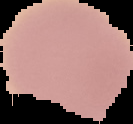
preparation = thin blood smear
image type = segmented cell region with the area outside set to black
malaria status = uninfected
image size = 133×124 pixels